Outline each Plasmodium falciparum-infected red blood cell.
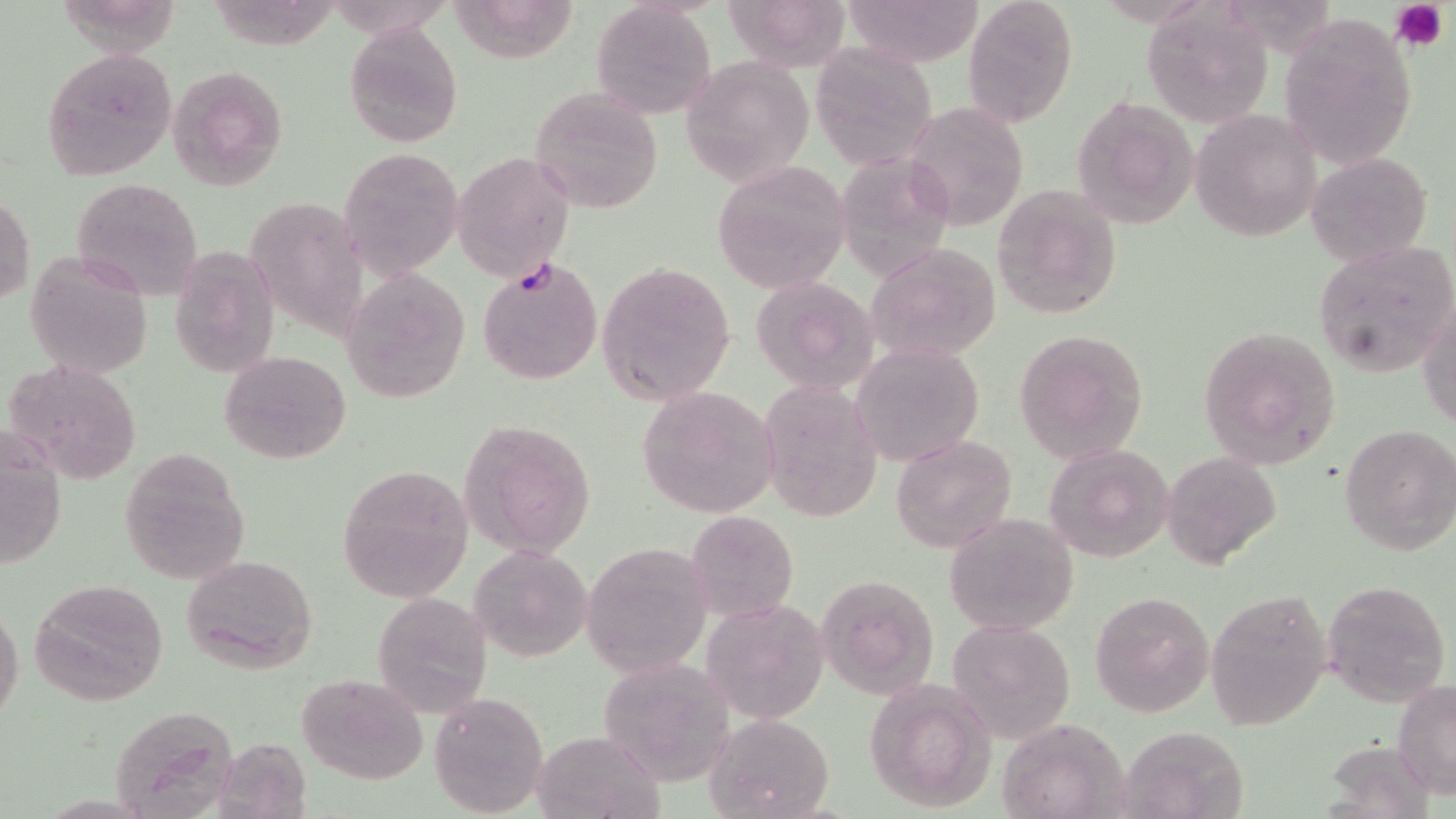
Approximate bounding boxes as [x1, y1, x2, y2] in pixels.
Plasmodium falciparum-infected red blood cells: [478, 255, 604, 386].

slide-level diagnosis = Plasmodium falciparum
magnification = 1000x
modality = light microscopy
platelet locations = approximate bounding boxes as [x1, y1, x2, y2] in pixels: [1392, 0, 1448, 50]
uninfected red blood cell locations = approximate bounding boxes as [x1, y1, x2, y2] in pixels: [449, 0, 583, 65], [725, 0, 851, 71], [843, 0, 987, 68], [962, 0, 1080, 127], [1141, 0, 1276, 129], [589, 3, 715, 119], [1280, 13, 1417, 173], [344, 22, 464, 148], [810, 40, 938, 172], [41, 48, 177, 180], [681, 55, 814, 188], [166, 65, 288, 191], [530, 87, 663, 214], [1072, 94, 1199, 231], [903, 102, 1031, 231], [1191, 110, 1320, 241], [340, 147, 464, 279], [451, 150, 576, 281], [1305, 150, 1433, 266], [712, 162, 850, 294], [69, 179, 203, 297], [992, 182, 1125, 319], [0, 193, 34, 307], [248, 193, 369, 343], [1312, 240, 1456, 376], [867, 243, 1002, 364], [172, 249, 280, 377], [25, 251, 152, 380], [595, 260, 736, 406], [342, 270, 472, 403], [751, 276, 878, 394], [1418, 299, 1455, 430], [1196, 325, 1342, 469], [1012, 328, 1149, 463], [852, 342, 984, 467], [220, 351, 350, 463], [6, 358, 144, 486], [757, 379, 882, 524], [636, 385, 781, 520], [458, 418, 598, 561], [1339, 422, 1455, 557], [2, 424, 67, 572], [890, 433, 1017, 552], [1042, 442, 1174, 561], [118, 448, 250, 584], [1163, 451, 1283, 571], [337, 464, 476, 602], [683, 509, 799, 625], [943, 511, 1079, 636], [580, 541, 714, 678], [470, 543, 593, 662], [181, 554, 319, 674], [817, 571, 942, 701], [1322, 576, 1451, 708], [28, 578, 169, 705], [1207, 587, 1333, 732], [1089, 590, 1217, 717], [371, 594, 492, 718], [0, 601, 22, 731], [715, 604, 831, 720], [947, 617, 1077, 744], [596, 655, 738, 786], [296, 673, 429, 785], [867, 677, 996, 812], [1393, 681, 1456, 797], [430, 692, 549, 816], [106, 707, 237, 814], [708, 712, 834, 818], [996, 719, 1133, 818], [1116, 727, 1253, 819], [532, 728, 663, 818], [217, 733, 319, 811]
stain = May-Grünwald-Giemsa
image size = 1456×819 pixels
field of view = single
preparation = thin blood film